Classify this cell by malaria status.
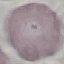
Uninfected.

capture = smartphone through the microscope eyepiece
stain = Giemsa
image type = cell patch, automatically extracted from a larger field of view and resized to 64 × 64 pixels
preparation = thin blood film